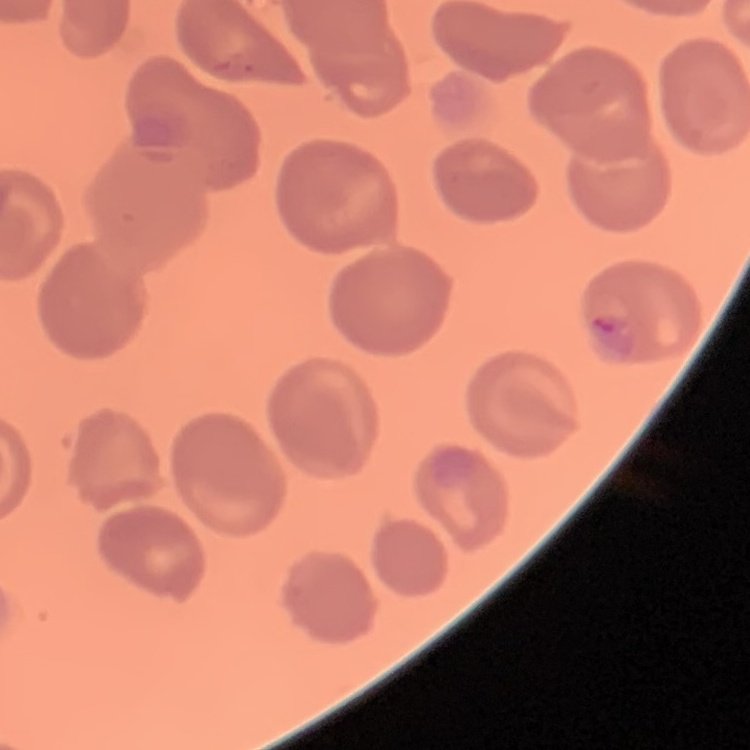

The erythrocytes show no rouleaux formation. Field's or Giemsa stain. Square crop of a larger photomicrograph. Thin blood film.